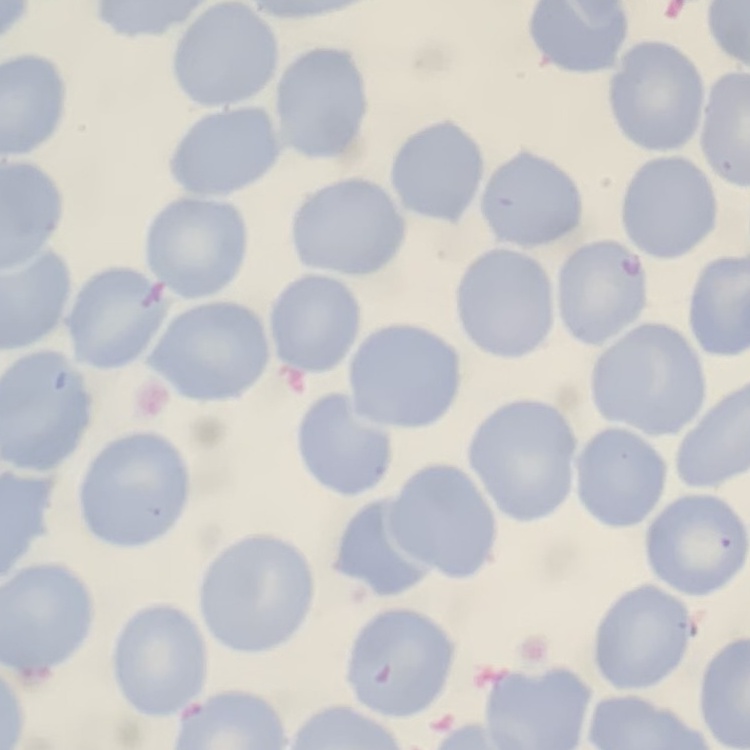

The red blood cells show no rouleaux formation. Field's or Giemsa stain. Square crop of a larger photomicrograph. Thin blood smear.